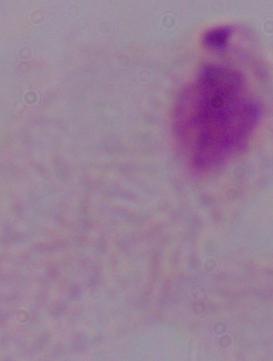

Summary:
  - Magnification: 1000x
  - Modality: micrograph
  - Identification: trichomonad